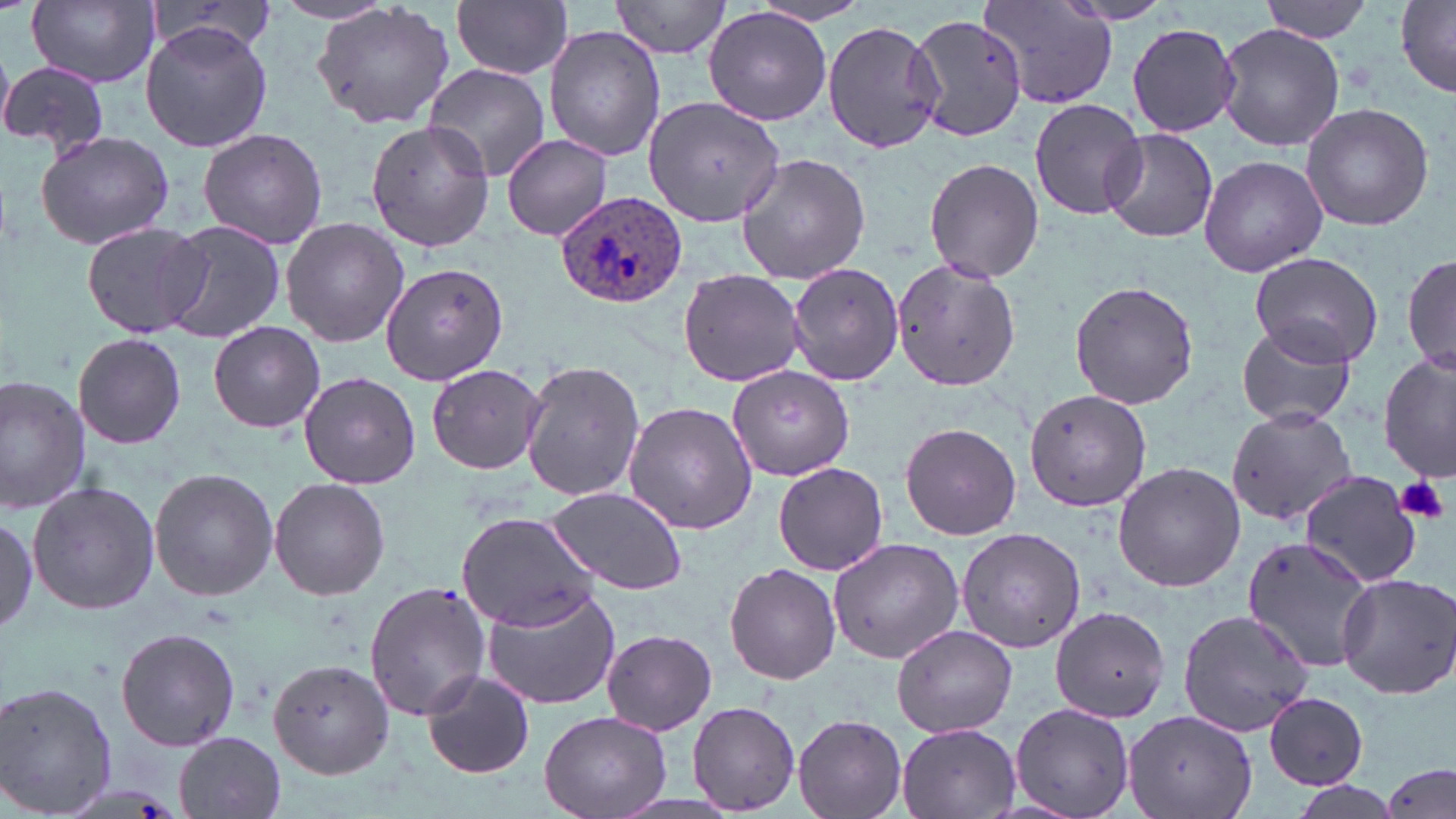

slide-level diagnosis = Plasmodium ovale
uninfected red blood cell locations = approximate bounding boxes as named x1/y1/x2/y2 corners in pixels: (x1=27, y1=0, x2=162, y2=88), (x1=269, y1=0, x2=395, y2=26), (x1=453, y1=0, x2=573, y2=79), (x1=609, y1=0, x2=734, y2=59), (x1=1259, y1=0, x2=1375, y2=43), (x1=981, y1=1, x2=1118, y2=111), (x1=312, y1=2, x2=457, y2=130), (x1=1397, y1=2, x2=1456, y2=95), (x1=703, y1=7, x2=833, y2=126), (x1=908, y1=12, x2=1028, y2=143), (x1=823, y1=20, x2=945, y2=154), (x1=140, y1=21, x2=272, y2=154), (x1=1215, y1=23, x2=1346, y2=152), (x1=1128, y1=24, x2=1239, y2=135), (x1=544, y1=26, x2=665, y2=160), (x1=0, y1=60, x2=109, y2=157), (x1=424, y1=63, x2=551, y2=179), (x1=643, y1=95, x2=786, y2=227), (x1=1029, y1=100, x2=1147, y2=218), (x1=1300, y1=101, x2=1435, y2=232), (x1=364, y1=118, x2=493, y2=251), (x1=1100, y1=126, x2=1218, y2=242), (x1=196, y1=128, x2=329, y2=248), (x1=34, y1=130, x2=174, y2=249), (x1=501, y1=134, x2=614, y2=239), (x1=733, y1=153, x2=872, y2=285), (x1=1198, y1=153, x2=1328, y2=278), (x1=924, y1=158, x2=1043, y2=284), (x1=280, y1=218, x2=408, y2=346), (x1=155, y1=219, x2=287, y2=345), (x1=80, y1=220, x2=210, y2=339), (x1=1250, y1=250, x2=1386, y2=370), (x1=1401, y1=250, x2=1454, y2=378), (x1=891, y1=258, x2=1022, y2=391), (x1=380, y1=259, x2=510, y2=387), (x1=787, y1=262, x2=905, y2=387), (x1=678, y1=267, x2=806, y2=388), (x1=1068, y1=280, x2=1200, y2=409), (x1=208, y1=321, x2=326, y2=433), (x1=1236, y1=321, x2=1357, y2=428), (x1=70, y1=333, x2=189, y2=448), (x1=1379, y1=354, x2=1454, y2=484), (x1=519, y1=358, x2=646, y2=503), (x1=427, y1=363, x2=546, y2=475), (x1=728, y1=364, x2=853, y2=482), (x1=299, y1=370, x2=421, y2=490), (x1=0, y1=375, x2=90, y2=514), (x1=1024, y1=390, x2=1150, y2=511), (x1=623, y1=402, x2=758, y2=535), (x1=1228, y1=404, x2=1357, y2=526), (x1=899, y1=423, x2=1021, y2=539), (x1=1112, y1=461, x2=1244, y2=592), (x1=772, y1=462, x2=887, y2=575), (x1=149, y1=466, x2=278, y2=602), (x1=1301, y1=472, x2=1424, y2=588), (x1=269, y1=477, x2=391, y2=601), (x1=27, y1=479, x2=160, y2=617), (x1=545, y1=486, x2=690, y2=597), (x1=456, y1=511, x2=600, y2=630), (x1=0, y1=514, x2=37, y2=634), (x1=956, y1=528, x2=1085, y2=651), (x1=1241, y1=534, x2=1375, y2=673), (x1=828, y1=539, x2=963, y2=662), (x1=724, y1=562, x2=841, y2=684), (x1=1336, y1=572, x2=1456, y2=700), (x1=364, y1=579, x2=491, y2=723), (x1=481, y1=585, x2=622, y2=710), (x1=1049, y1=606, x2=1169, y2=723), (x1=1177, y1=609, x2=1315, y2=735), (x1=892, y1=624, x2=1019, y2=738), (x1=116, y1=627, x2=240, y2=752), (x1=601, y1=628, x2=717, y2=736), (x1=267, y1=658, x2=399, y2=780), (x1=421, y1=671, x2=535, y2=779), (x1=1, y1=679, x2=119, y2=819), (x1=1262, y1=691, x2=1370, y2=791), (x1=687, y1=701, x2=801, y2=815), (x1=1010, y1=701, x2=1136, y2=819), (x1=1124, y1=708, x2=1260, y2=819), (x1=539, y1=709, x2=670, y2=818), (x1=792, y1=714, x2=907, y2=819), (x1=896, y1=723, x2=1023, y2=819), (x1=172, y1=732, x2=285, y2=817), (x1=1381, y1=761, x2=1453, y2=819), (x1=1284, y1=781, x2=1407, y2=819)
stain = May-Grünwald-Giemsa
magnification = 1000x
image size = 1456×819 pixels
Plasmodium ovale-infected red blood cell locations = approximate bounding boxes as named x1/y1/x2/y2 corners in pixels: (x1=555, y1=190, x2=688, y2=311)
platelet locations = approximate bounding boxes as named x1/y1/x2/y2 corners in pixels: (x1=1395, y1=475, x2=1450, y2=525)
modality = light microscopy
preparation = thin blood smear
field of view = one of a larger specimen